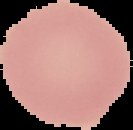

Summary:
  - Image size: 133×130 pixels
  - Malaria status: uninfected
  - Image type: cell region segmented out of the field of view; surrounding area masked to black
  - Preparation: thin blood film